Locate every blood parasite and identify its species.
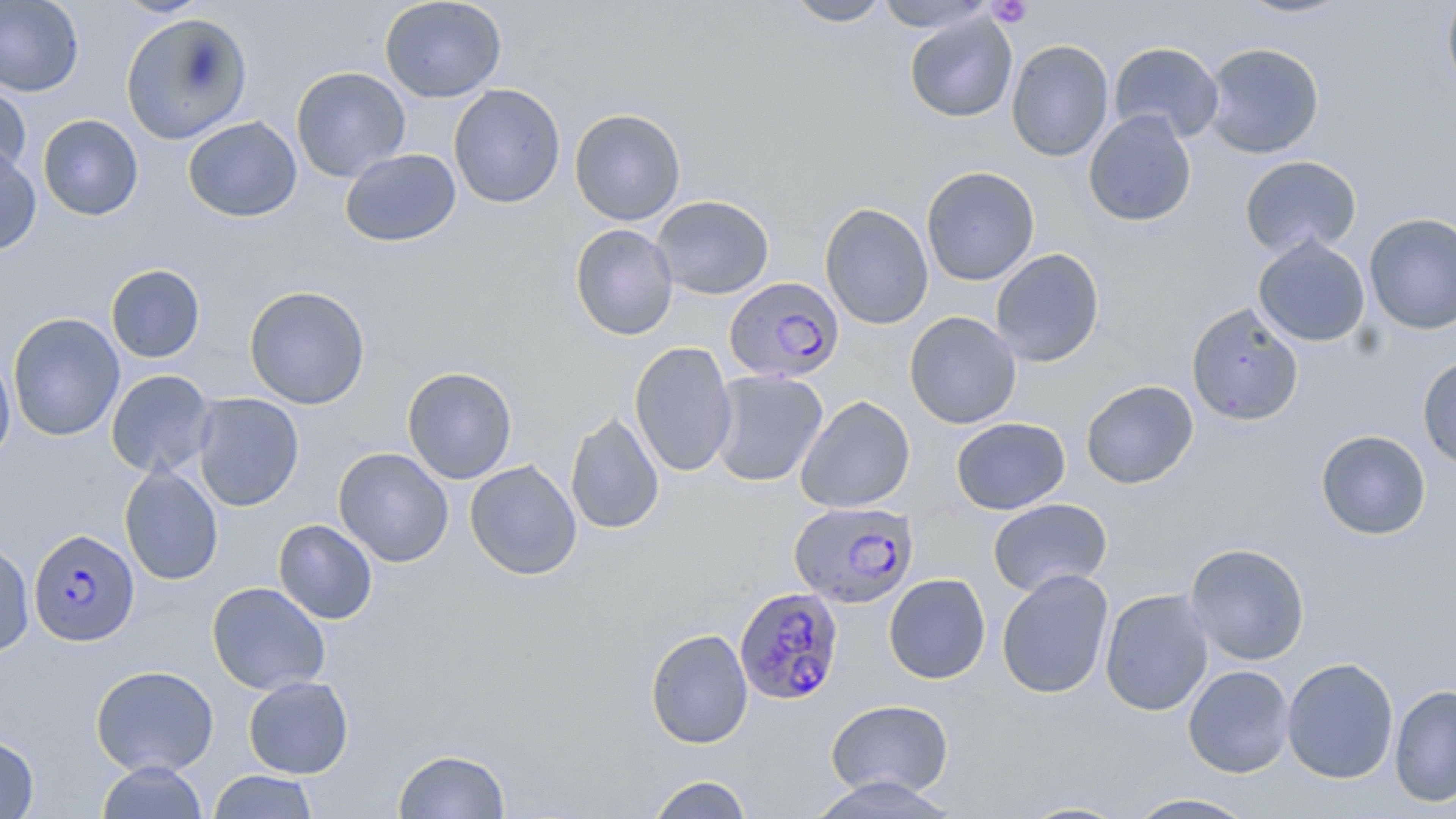
Approximate bounding boxes as (x1,y1)-(x2,y2) corner pairs in pixels.
Plasmodium falciparum-infected red blood cells: (726,275)-(847,386), (789,500)-(919,608), (28,528)-(140,647), (734,587)-(845,705).
No Plasmodium ovale, Plasmodium malariae, Plasmodium vivax, Babesia divergens, or Trypanosoma brucei observed.

Platelet locations: (988,0)-(1033,28). Uninfected red blood cell locations: (111,0)-(213,18), (379,0)-(507,103), (782,0)-(893,27), (874,0)-(996,32), (1232,0)-(1358,19), (0,1)-(84,97), (1441,1)-(1456,101), (120,12)-(252,145), (904,13)-(1018,123), (1006,39)-(1114,162), (1108,42)-(1224,144), (1202,42)-(1325,159), (290,66)-(411,183), (0,78)-(32,180), (448,83)-(566,208), (569,108)-(686,226), (1083,109)-(1197,227), (37,114)-(144,220), (182,116)-(303,222), (0,145)-(42,255), (339,148)-(461,247), (1239,155)-(1362,258), (920,167)-(1040,286), (651,194)-(775,300), (820,202)-(934,330), (1364,212)-(1456,335), (569,223)-(678,340), (1252,234)-(1371,348), (990,248)-(1105,368), (105,264)-(206,363), (243,285)-(371,409), (1186,302)-(1305,427), (904,311)-(1021,429), (7,312)-(125,442), (629,341)-(738,477), (0,350)-(16,469), (1417,354)-(1456,470), (402,366)-(518,484), (106,370)-(217,478), (709,370)-(828,487), (1080,380)-(1199,490), (192,393)-(304,512), (795,395)-(915,513), (565,411)-(664,535), (951,417)-(1070,515), (1315,429)-(1431,540), (333,447)-(454,567), (464,460)-(582,580), (119,464)-(223,585), (988,498)-(1113,597), (273,519)-(378,624), (0,540)-(35,657), (1185,542)-(1310,666), (996,568)-(1114,699), (883,573)-(991,684), (206,582)-(331,696), (1099,588)-(1214,717), (645,628)-(753,749), (1281,657)-(1399,784), (90,665)-(219,777), (1182,665)-(1295,778), (242,675)-(354,778), (1388,684)-(1456,808), (826,699)-(954,799), (0,734)-(39,818), (393,748)-(511,818), (96,761)-(209,819), (207,770)-(319,818), (645,774)-(755,819), (808,776)-(960,817), (1124,792)-(1261,818), (1013,798)-(1137,818). Slide-level diagnosis: Plasmodium falciparum. Single field of view. Thin blood smear. Image is 1456×819 pixels. May-Grünwald-Giemsa stain. 1000x magnification. Light microscopy.